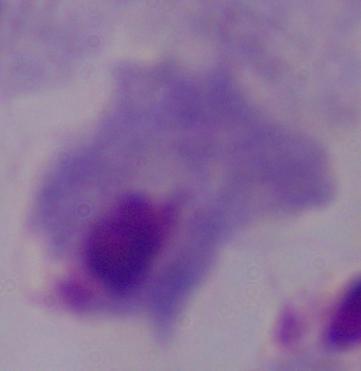

modality = photomicrograph
magnification = 1000x
identification = trichomonad